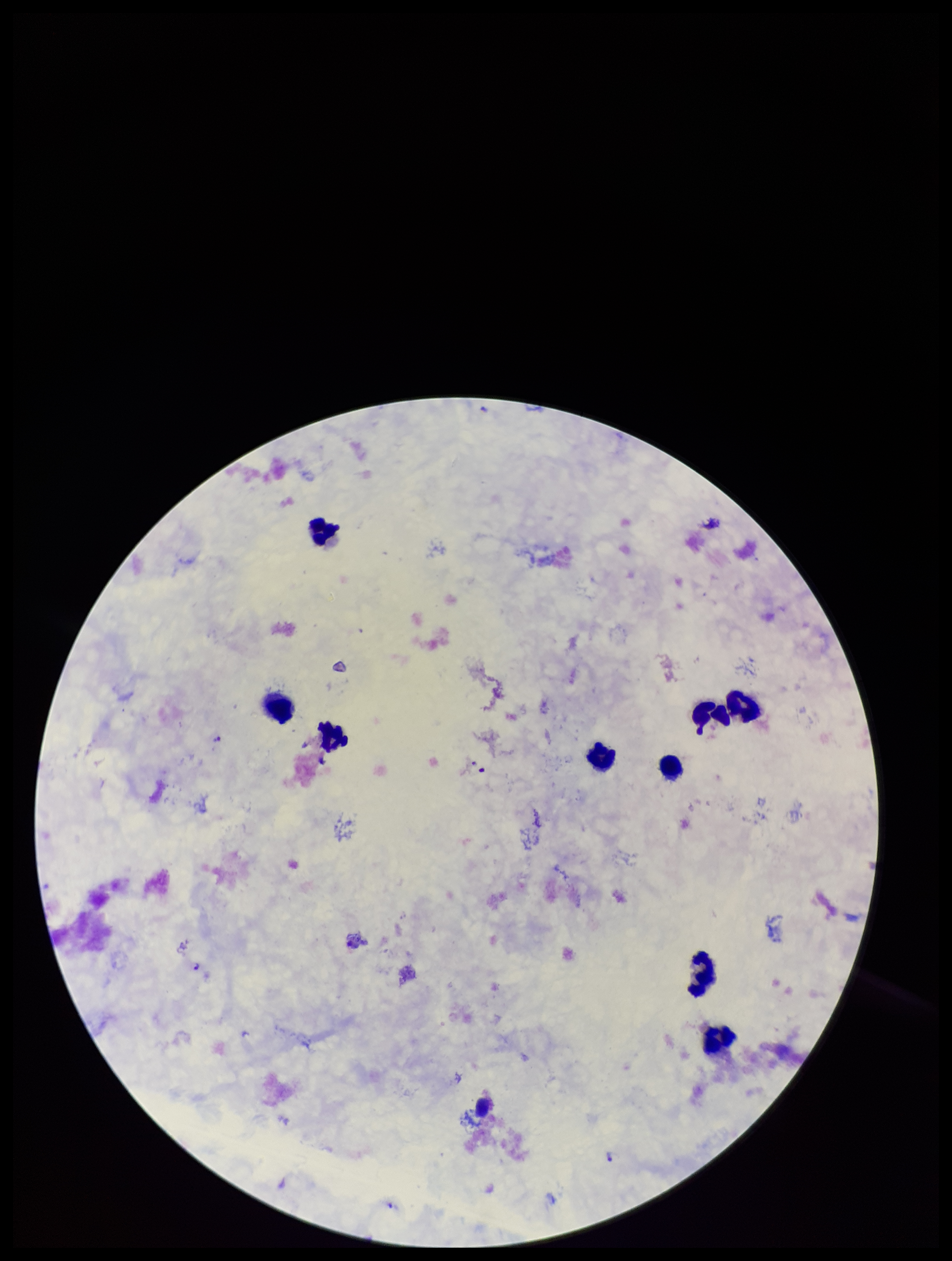 Plasmodium parasites: seen. Parasite count: 4. Patient malaria status: positive. Leukocyte count: 9. Giemsa stain. Image is 952×1261 pixels. Species reported for this patient: Plasmodium falciparum. Preparation: thick. Smartphone photograph taken through the eyepiece of a microscope. Single field of view.